Report the malaria status of this cell.
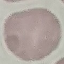

Uninfected.

Automatically extracted cell patch, resized to 64 × 64 pixels. Photographed with a smartphone camera at the microscope eyepiece. Thin smear of blood. Giemsa stain.